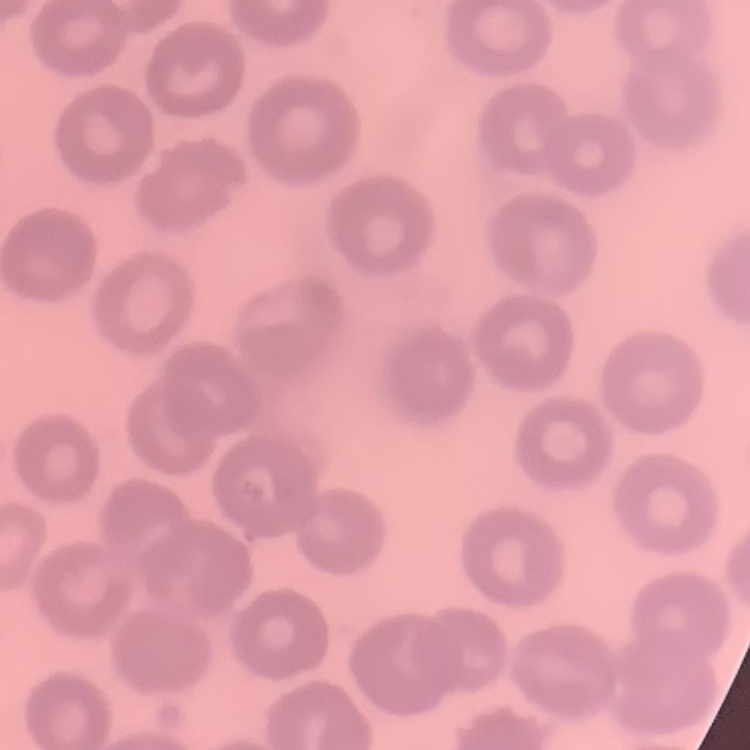
Summary:
  - Red blood cell morphology: no rouleaux formation
  - Image type: square crop of a larger photomicrograph
  - Preparation: thin peripheral smear
  - Stain: Field's or Giemsa